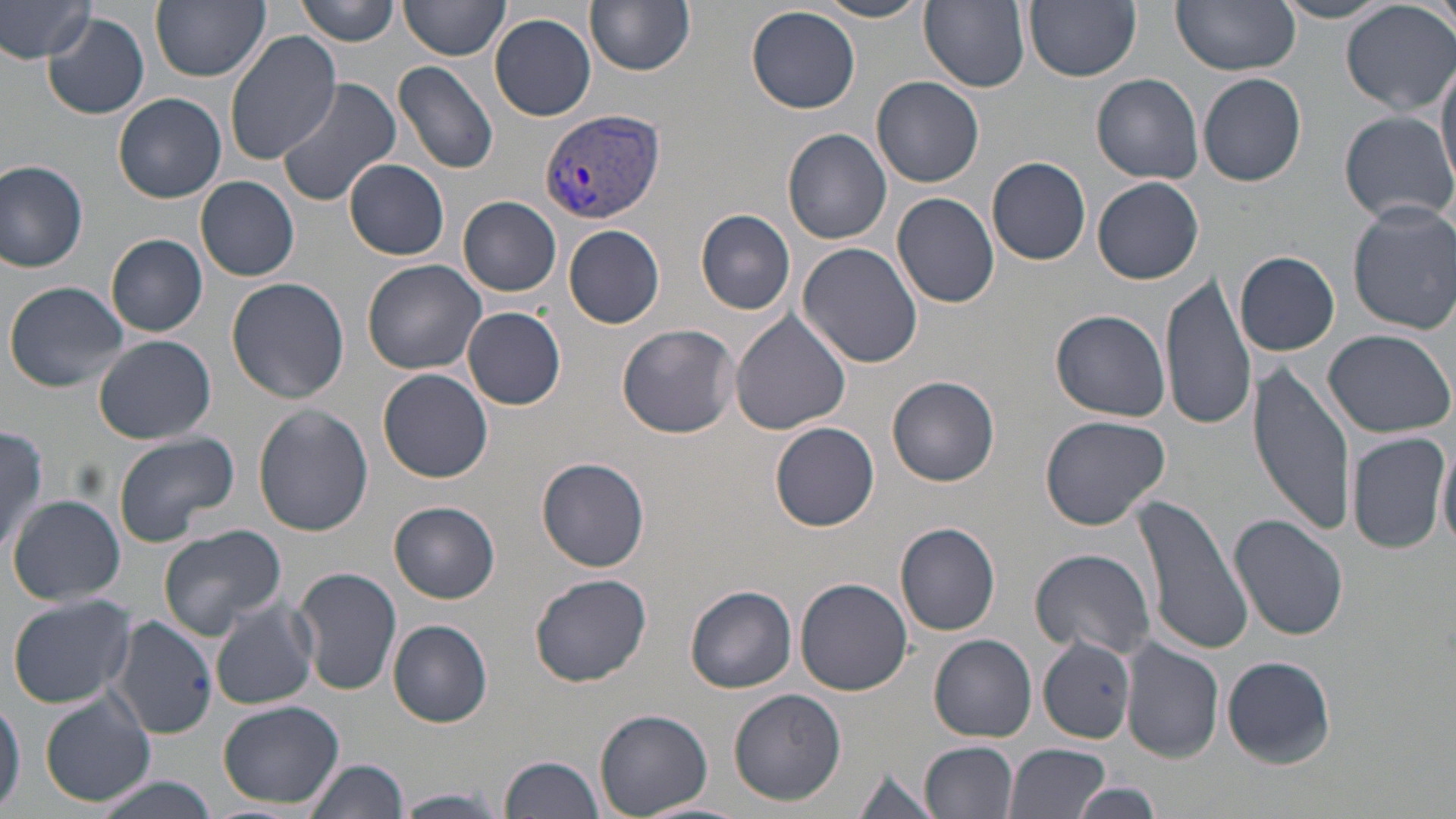
Approximate bounding boxes as (x1,y1)-(x2,y2) corner pairs in pixels. Plasmodium vivax-infected red blood cell locations: (540,111)-(665,222). Uninfected red blood cell locations: (0,0)-(100,67), (151,0)-(270,82), (297,0)-(400,46), (399,0)-(510,60), (588,0)-(696,75), (809,0)-(932,23), (919,0)-(1031,91), (1024,0)-(1141,81), (1172,0)-(1301,75), (1341,0)-(1455,115), (1272,1)-(1393,23), (1427,1)-(1454,42), (747,5)-(861,113), (42,12)-(149,119), (490,14)-(595,121), (224,29)-(341,164), (1437,55)-(1456,192), (393,59)-(500,174), (1199,73)-(1308,187), (873,74)-(985,187), (1092,74)-(1205,183), (274,77)-(403,207), (113,93)-(227,203), (1338,111)-(1455,226), (782,128)-(892,244), (0,157)-(91,272), (988,157)-(1091,265), (345,158)-(449,259), (195,174)-(300,280), (1093,176)-(1205,284), (892,192)-(1000,309), (459,196)-(563,297), (1348,202)-(1456,334), (696,210)-(796,314), (564,223)-(665,328), (106,234)-(208,337), (798,242)-(923,367), (1235,252)-(1339,355), (361,259)-(489,375), (1162,271)-(1259,433), (226,276)-(350,405), (5,280)-(130,393), (462,307)-(567,410), (730,309)-(852,435), (1052,310)-(1172,422), (618,324)-(739,438), (1322,328)-(1454,438), (93,335)-(218,444), (1248,363)-(1356,536), (378,368)-(494,482), (888,376)-(1000,486), (253,403)-(374,538), (1040,414)-(1171,529), (770,422)-(880,532), (0,426)-(50,556), (111,432)-(241,548), (1347,432)-(1450,556), (1435,438)-(1456,554), (535,457)-(652,572), (1133,491)-(1253,657), (7,494)-(125,606), (388,501)-(501,604), (1229,514)-(1349,642), (895,522)-(1002,636), (155,526)-(288,641), (1029,547)-(1155,659), (295,566)-(402,696), (528,572)-(653,686), (794,576)-(913,696), (684,584)-(797,695), (8,593)-(134,708), (208,598)-(319,711), (114,615)-(218,740), (387,620)-(494,727), (930,635)-(1036,743), (1037,636)-(1136,743), (1122,641)-(1224,764), (1221,655)-(1337,767), (728,689)-(847,804), (40,692)-(155,808), (0,697)-(24,816), (217,700)-(347,809), (595,708)-(712,817), (920,740)-(1019,818), (1003,742)-(1111,819), (500,754)-(608,819), (306,759)-(409,819), (851,767)-(943,819), (92,777)-(219,818), (1072,782)-(1164,818), (395,790)-(507,817). Slide-level diagnosis: Plasmodium vivax. May-Grünwald-Giemsa stain. Light microscopy. Image is 1456×819 pixels. Thin blood film. Captured at 1000x magnification. One field of a larger specimen.